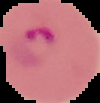

image type = segmented cell region with the area outside set to black
image size = 100×103 pixels
result = Plasmodium parasites detected
preparation = thin blood smear